Point out each Plasmodium parasite.
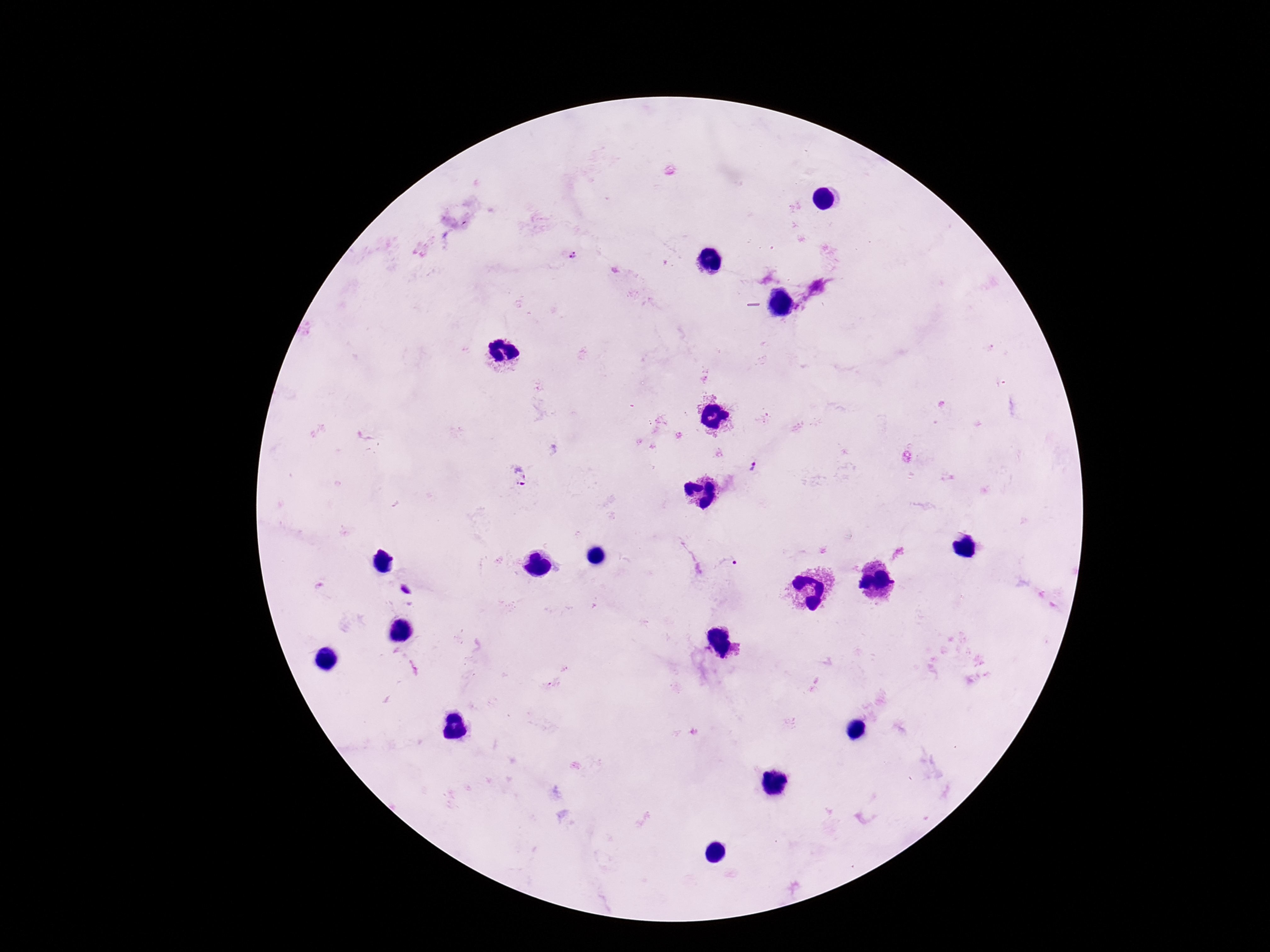

Approximate centers as {x, y} in pixels.
Plasmodium parasites: {572, 255}, {798, 308}, {755, 467}, {519, 476}, {728, 565}, {564, 669}, {553, 684}.

stain = Giemsa
magnification = 100x
patient malaria status = positive
field of view = one from this slide
preparation = thick peripheral-blood smear
image size = 1270×952 pixels
capture = smartphone camera through the microscope eyepiece